Name the cell type shown.
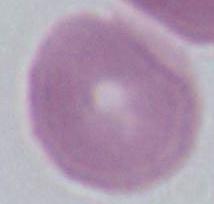

This is an erythrocyte.

magnification = 1000x
modality = photomicrograph